Name the parasite shown.
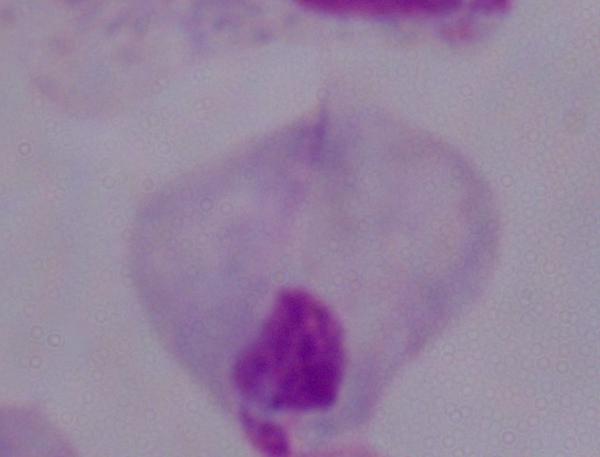

This is a trichomonad.

{
  "modality": "photomicrograph",
  "magnification": "1000x"
}